Report the malaria status of this cell.
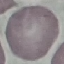
It is uninfected.

Summary:
  - Capture: smartphone camera at the microscope eyepiece
  - Image type: automatically extracted cell patch, resized to 64 × 64 pixels
  - Stain: Giemsa
  - Preparation: thin blood film